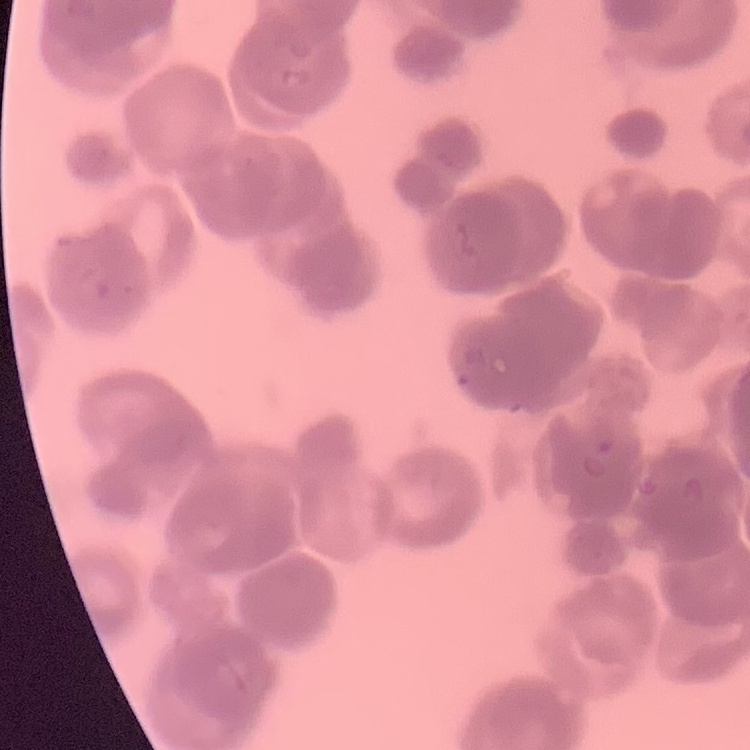
erythrocyte morphology = rouleaux formation
stain = Field's or Giemsa
preparation = thin peripheral smear
image type = one tile cut from a larger photomicrograph